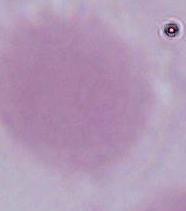

identification = red blood cell
magnification = 1000x
modality = micrograph